Outline each blood parasite and name the species.
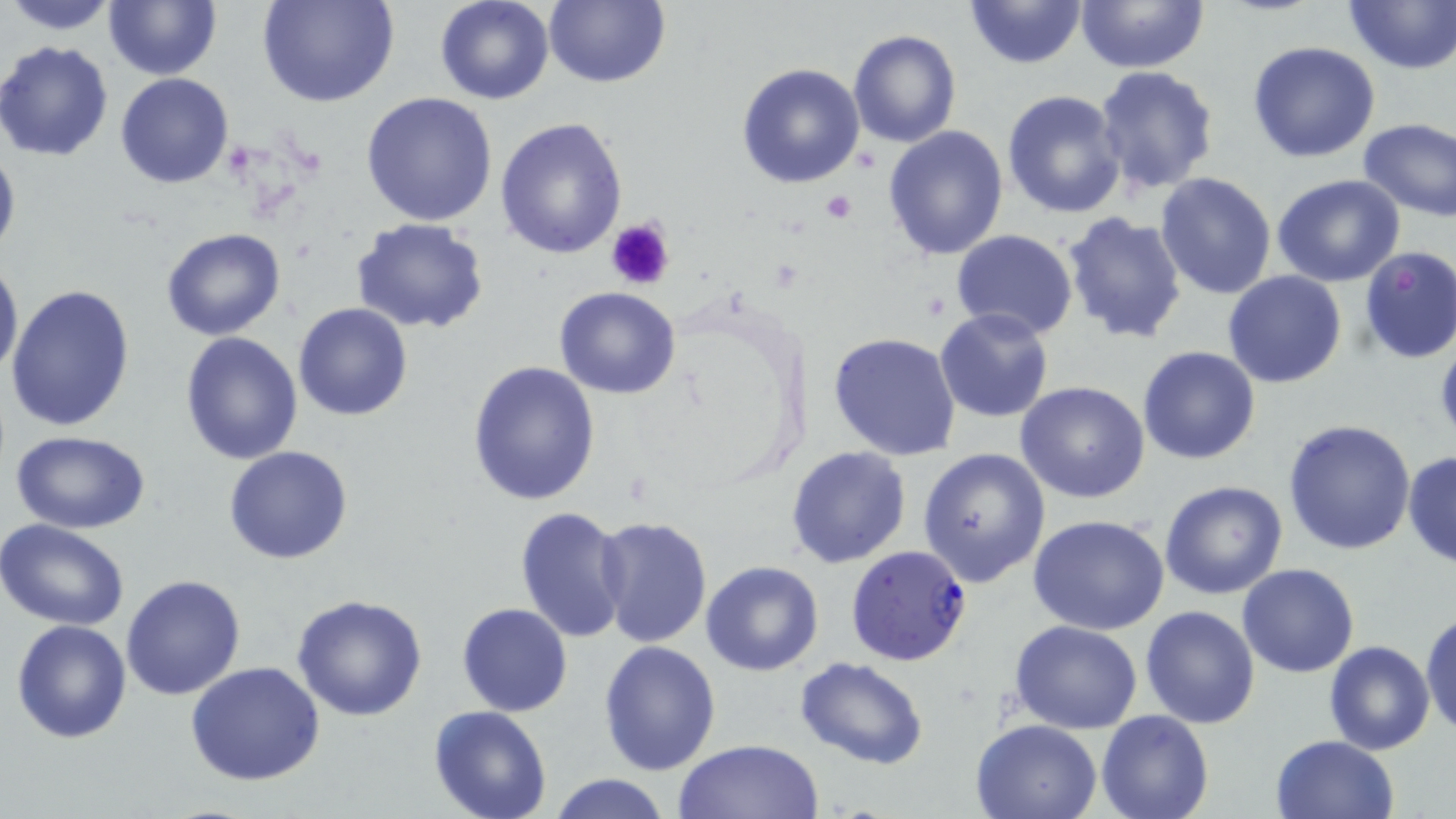

Approximate bounding boxes as (x1, y1, x2, y2) in pixels.
Plasmodium falciparum-infected red blood cells: (845, 544, 973, 667).
No Plasmodium ovale, Plasmodium malariae, Plasmodium vivax, Babesia divergens, or Trypanosoma brucei observed.

Platelet locations: (819, 188, 857, 224), (606, 216, 675, 291). Uninfected red blood cell locations: (4, 0, 121, 35), (103, 0, 220, 80), (258, 0, 401, 109), (434, 0, 557, 106), (544, 0, 670, 88), (963, 0, 1088, 70), (1342, 0, 1454, 73), (1075, 2, 1208, 74), (847, 29, 961, 147), (0, 40, 115, 163), (1246, 41, 1380, 163), (736, 62, 866, 189), (1093, 65, 1218, 193), (115, 73, 235, 189), (1002, 89, 1127, 218), (360, 93, 499, 228), (495, 116, 628, 260), (1356, 118, 1455, 221), (882, 126, 1009, 261), (0, 139, 20, 267), (1153, 171, 1276, 300), (1271, 175, 1405, 289), (1060, 211, 1189, 347), (350, 216, 490, 333), (161, 228, 286, 342), (950, 230, 1080, 342), (1357, 245, 1456, 363), (0, 255, 23, 381), (1222, 269, 1347, 388), (5, 282, 137, 433), (554, 286, 682, 399), (293, 302, 413, 422), (935, 308, 1054, 423), (180, 330, 304, 465), (830, 332, 962, 461), (1136, 346, 1261, 465), (467, 362, 602, 505), (1016, 381, 1150, 502), (1283, 418, 1418, 556), (9, 429, 154, 531), (224, 446, 353, 564), (786, 446, 910, 568), (919, 448, 1051, 588), (1403, 449, 1456, 568), (1158, 480, 1288, 601), (515, 507, 631, 646), (593, 515, 713, 650), (1028, 515, 1172, 637), (0, 520, 130, 632), (700, 562, 823, 677), (1236, 563, 1360, 677), (120, 573, 246, 701), (291, 595, 428, 722), (458, 603, 572, 716), (1139, 605, 1260, 729), (1421, 609, 1455, 737), (11, 618, 133, 743), (1010, 621, 1143, 733), (598, 639, 722, 776), (1323, 641, 1435, 755), (795, 657, 930, 769), (186, 662, 329, 787), (429, 707, 554, 819), (1097, 709, 1213, 819), (973, 718, 1101, 819), (1269, 735, 1400, 819), (672, 740, 824, 819), (547, 774, 672, 819). Slide-level diagnosis: Plasmodium falciparum. Thin blood smear. Light microscopy. May-Grünwald-Giemsa stain. 1000x magnification. Image is 1456×819 pixels. One field of a larger specimen.